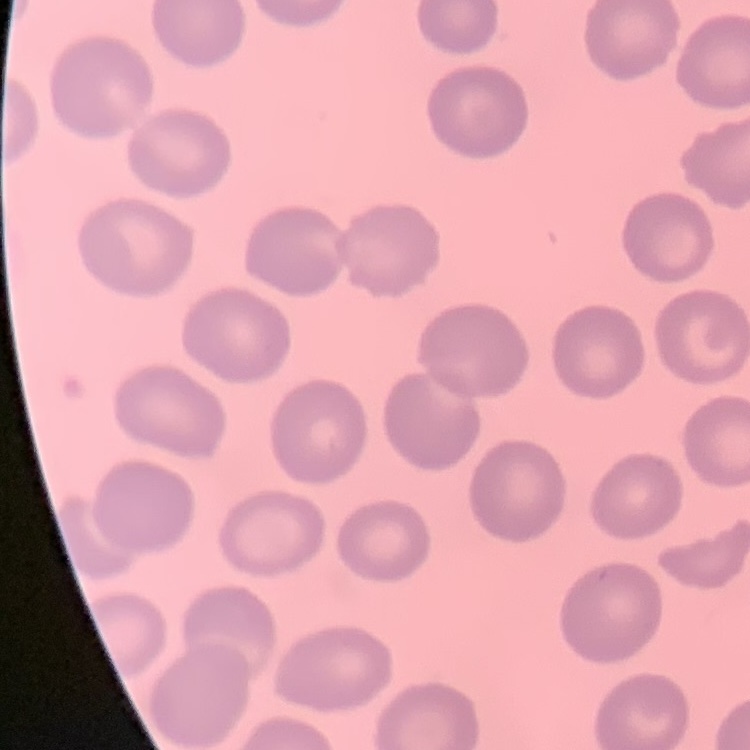

The erythrocytes exhibit no rouleaux formation. Thin peripheral smear. One tile cut from a larger photomicrograph. Stained with either Field's or Giemsa.